Point out each leukocyte.
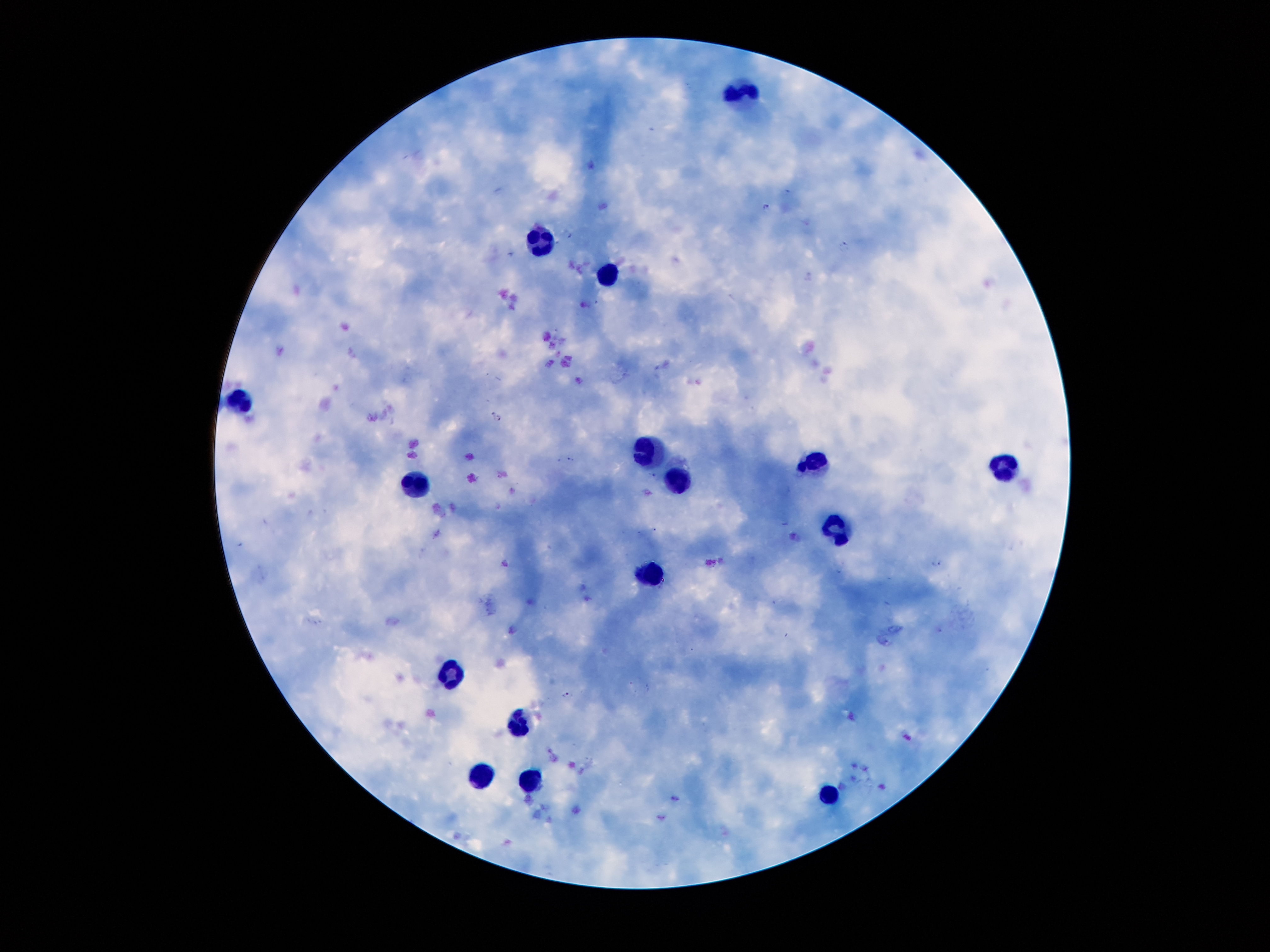
Approximate centers as {x, y} in pixels.
Leukocytes: {735, 96}, {537, 243}, {607, 271}, {243, 404}, {648, 447}, {813, 460}, {1004, 469}, {678, 481}, {417, 486}, {837, 528}, {654, 576}, {454, 678}, {517, 726}, {481, 777}, {531, 781}, {827, 794}.

Plasmodium parasite locations = {767, 206}, {567, 232}, {845, 245}, {493, 415}, {571, 457}, {653, 474}, {937, 563}, {566, 694}
preparation = thick blood film
field of view = one from this slide
stain = Giemsa
image size = 1270×952 pixels
capture = smartphone camera through the microscope eyepiece
magnification = 100x
patient malaria status = positive for Plasmodium falciparum